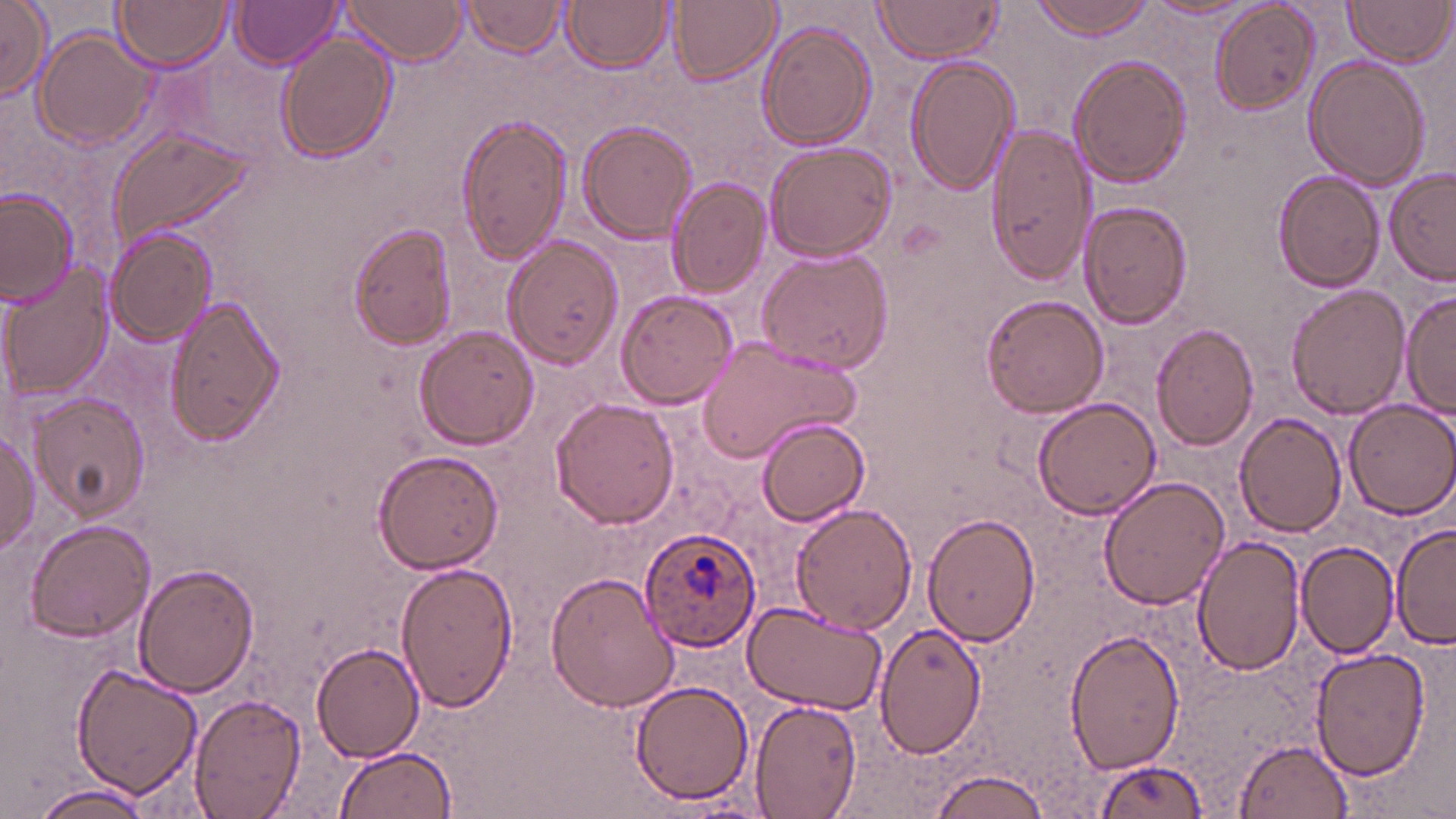

Approximate bounding boxes as (x1, y1, x2, y2) in pixels. Uninfected red blood cell locations: (114, 0, 232, 71), (336, 0, 469, 64), (669, 0, 782, 86), (1029, 0, 1159, 39), (1211, 0, 1322, 114), (235, 1, 344, 70), (869, 1, 1008, 63), (1142, 1, 1255, 23), (1344, 1, 1451, 68), (0, 2, 53, 101), (461, 2, 570, 59), (565, 2, 671, 72), (758, 20, 877, 154), (33, 29, 157, 151), (277, 33, 396, 161), (905, 53, 1015, 196), (1069, 54, 1192, 189), (1304, 57, 1429, 190), (458, 111, 574, 266), (578, 120, 698, 243), (983, 120, 1097, 286), (107, 125, 258, 253), (763, 139, 900, 262), (1384, 166, 1456, 283), (1273, 172, 1385, 292), (667, 178, 768, 298), (0, 188, 79, 307), (1082, 200, 1192, 330), (349, 224, 459, 349), (107, 226, 215, 346), (505, 236, 624, 370), (758, 247, 894, 375), (6, 260, 118, 395), (1286, 283, 1410, 418), (0, 286, 16, 413), (1401, 288, 1455, 422), (616, 289, 740, 409), (981, 294, 1107, 418), (163, 295, 286, 445), (1151, 321, 1261, 450), (414, 325, 539, 449), (697, 336, 863, 468), (28, 392, 149, 523), (551, 397, 680, 530), (1032, 398, 1162, 519), (1342, 398, 1456, 518), (1234, 414, 1346, 537), (757, 418, 870, 527), (0, 427, 40, 555), (374, 450, 506, 574), (1098, 476, 1229, 611), (791, 504, 917, 634), (923, 510, 1042, 648), (22, 520, 156, 643), (1393, 524, 1455, 650), (1191, 534, 1306, 674), (1297, 541, 1401, 659), (397, 560, 519, 712), (133, 565, 259, 699), (547, 570, 680, 711), (739, 599, 887, 713), (877, 621, 988, 758), (1066, 628, 1186, 774), (312, 641, 426, 764), (1309, 647, 1430, 782), (71, 660, 205, 799), (629, 679, 756, 806), (189, 693, 306, 818), (747, 699, 862, 818), (1234, 739, 1355, 818), (333, 745, 457, 819), (1085, 758, 1210, 819), (925, 765, 1055, 819), (25, 782, 157, 819), (657, 796, 773, 818). Plasmodium ovale-infected red blood cell locations: (637, 527, 762, 651). Slide-level diagnosis: Plasmodium ovale. Captured at 1000x magnification. Thin blood film. Single field of view. Image is 1456×819 pixels. May-Grünwald-Giemsa-stained preparation. Light microscopy.